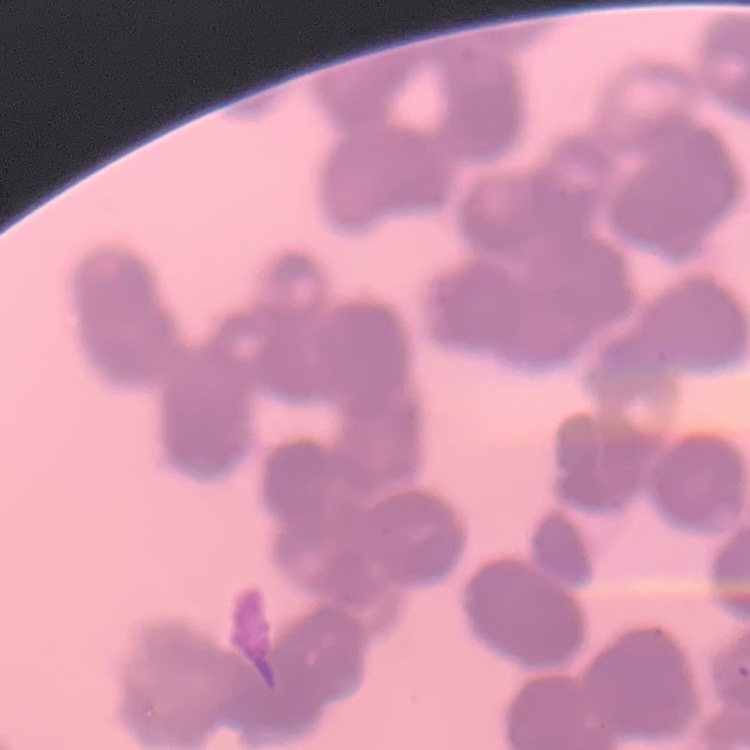 The erythrocytes show rouleaux formation. One tile cut from a larger photomicrograph. Field's or Giemsa stain. Thin blood smear.